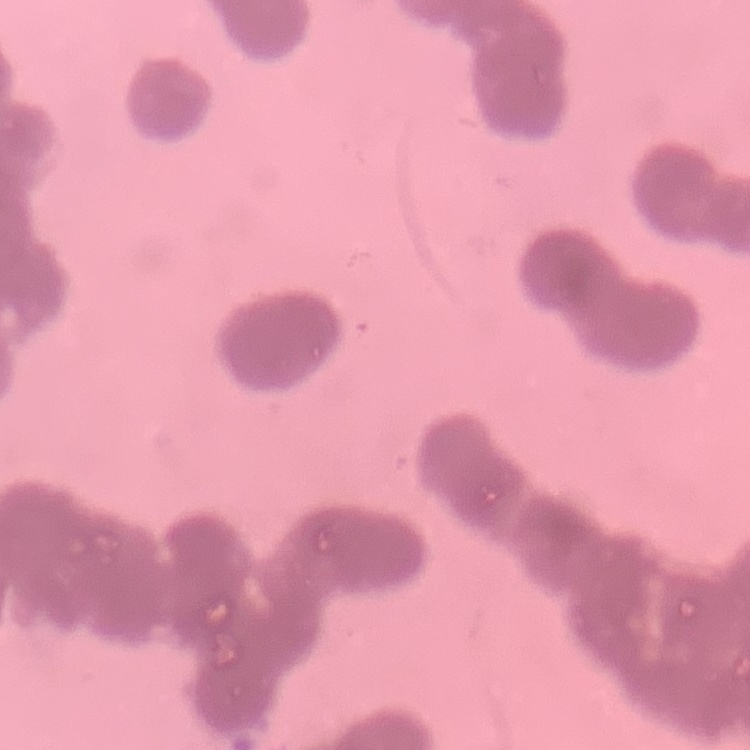

The erythrocytes show rouleaux formation. Field's or Giemsa stain. Square crop of a larger photomicrograph. Thin blood smear.